Comment on the morphology of the erythrocytes.
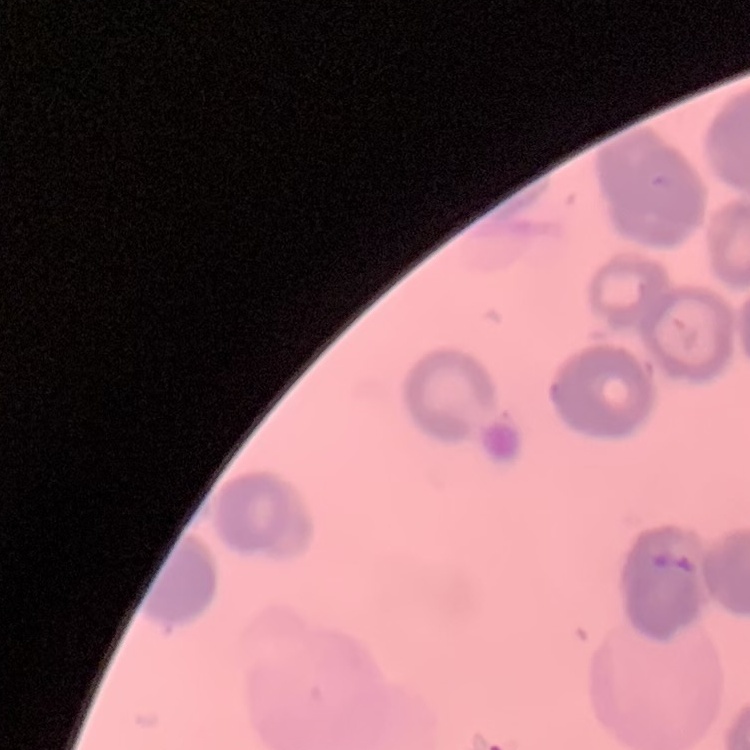
They show rouleaux formation.

One tile cut from a larger photomicrograph. Field's or Giemsa stain. Thin blood smear.